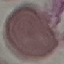
Malaria status: uninfected. Giemsa stain. Cell patch, automatically extracted from a larger field of view and resized to 64 × 64 pixels. Thin smear of blood. Photographed with a smartphone camera at the microscope eyepiece.